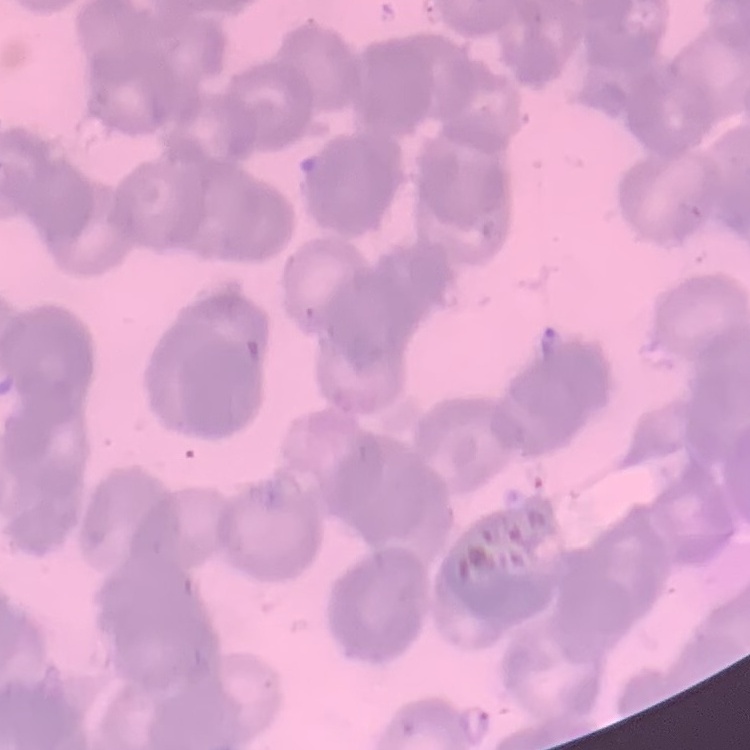

Summary:
  - Erythrocyte morphology: rouleaux formation
  - Stain: Field's or Giemsa
  - Preparation: thin peripheral smear
  - Image type: square crop of a larger photomicrograph